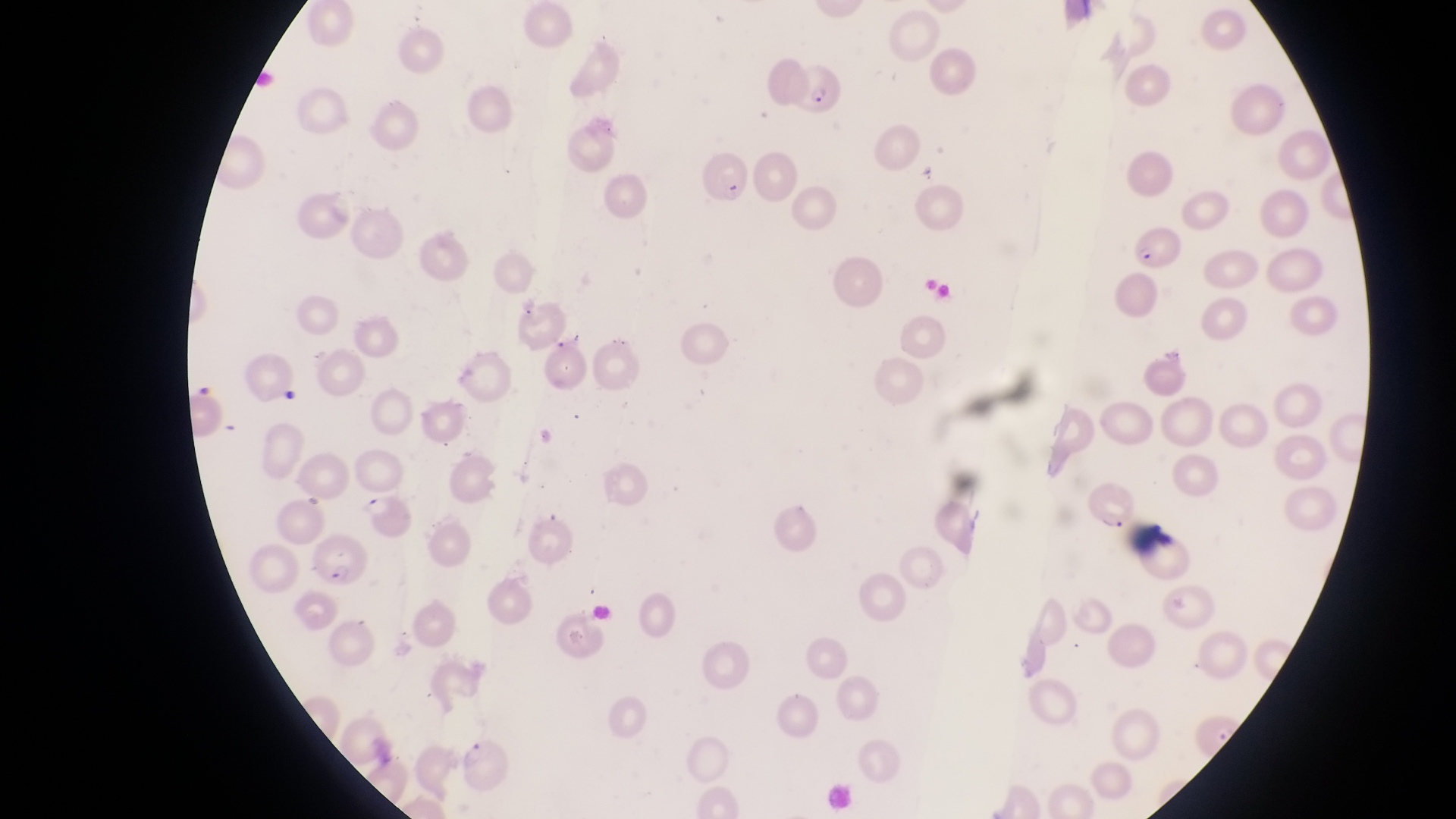 Approximate bounding boxes as [left, top, right, bottom] in pixels. Parasitised red blood cell locations: [782, 60, 843, 116], [700, 143, 749, 202], [1128, 221, 1184, 270], [1086, 476, 1136, 529], [304, 532, 368, 591]. Captured by a smartphone held over the eyepiece of an Olympus CX-23 microscope. Magnification of 1000x. Image is 1456×819 pixels. Thin blood film. Single field of view. Sample from Uganda.